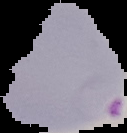
image type = segmented cell region on a black background
result = malaria parasites detected
preparation = thin blood film
image size = 127×133 pixels